Assess the morphology of the erythrocytes.
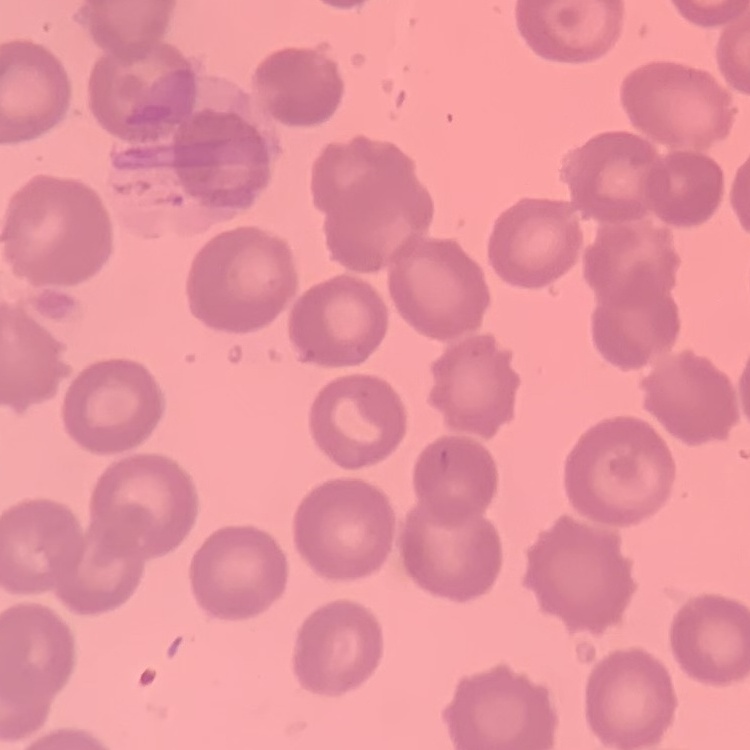

No rouleaux formation.

image type = one tile cut from a larger photomicrograph
stain = Field's or Giemsa
preparation = thin peripheral smear